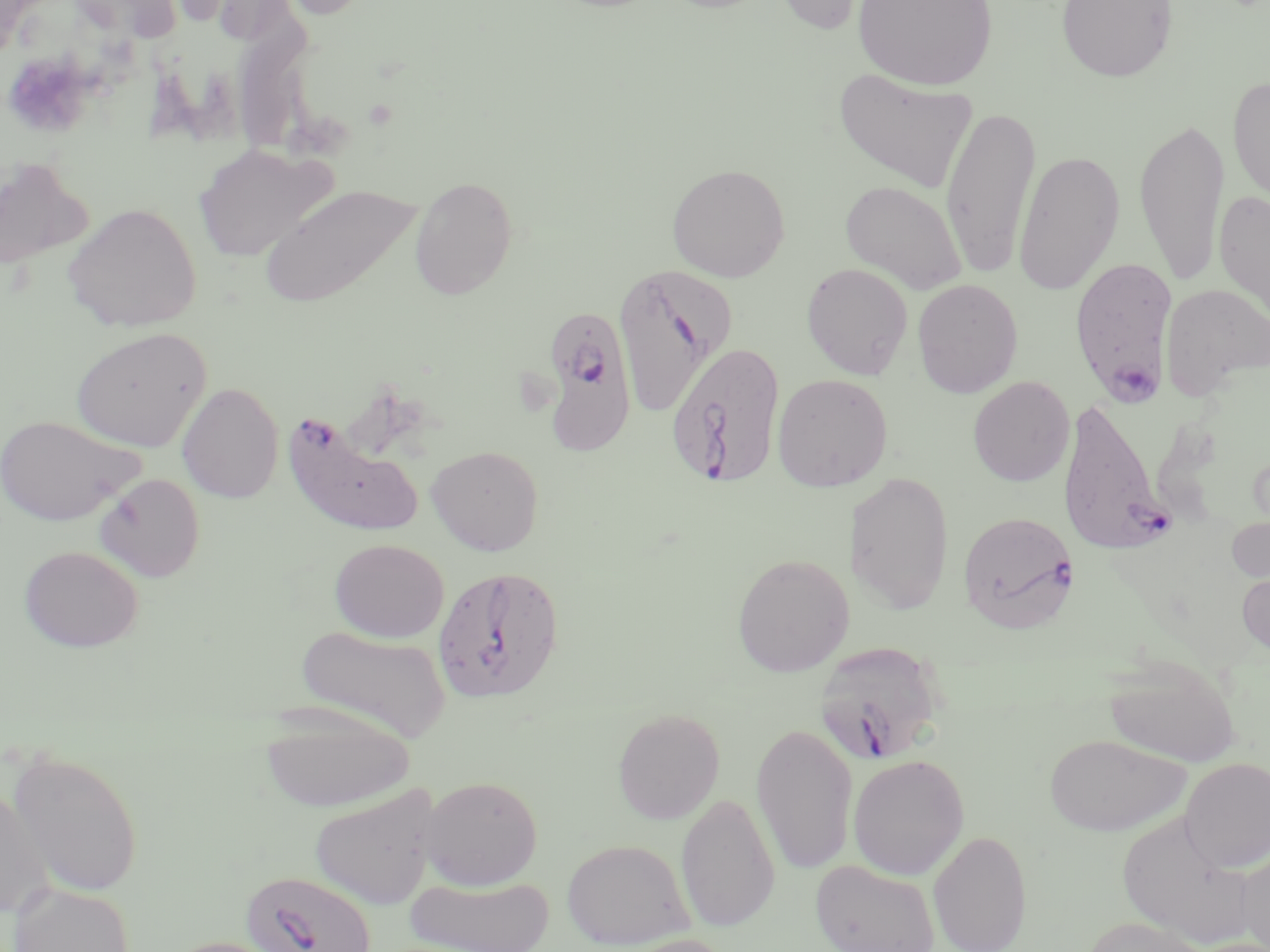

Approximate bounding boxes as named x1/y1/x2/y2 corners in pixels. Platelet locations: (x1=3, y1=51, x2=96, y2=137). Plasmodium falciparum-infected red blood cell locations: (x1=1069, y1=256, x2=1178, y2=403), (x1=612, y1=263, x2=736, y2=416), (x1=538, y1=312, x2=644, y2=462), (x1=666, y1=340, x2=787, y2=489), (x1=1057, y1=396, x2=1176, y2=555), (x1=283, y1=414, x2=424, y2=535), (x1=958, y1=510, x2=1080, y2=633), (x1=431, y1=565, x2=565, y2=703), (x1=814, y1=640, x2=947, y2=766), (x1=239, y1=869, x2=377, y2=952). Uninfected red blood cell locations: (x1=67, y1=0, x2=181, y2=42), (x1=768, y1=0, x2=887, y2=35), (x1=853, y1=0, x2=998, y2=90), (x1=1056, y1=0, x2=1177, y2=82), (x1=834, y1=68, x2=978, y2=194), (x1=1228, y1=74, x2=1270, y2=214), (x1=940, y1=105, x2=1041, y2=279), (x1=1134, y1=116, x2=1230, y2=288), (x1=193, y1=143, x2=337, y2=262), (x1=1013, y1=149, x2=1125, y2=297), (x1=0, y1=158, x2=91, y2=271), (x1=667, y1=162, x2=790, y2=281), (x1=409, y1=176, x2=518, y2=300), (x1=841, y1=180, x2=967, y2=294), (x1=261, y1=183, x2=421, y2=308), (x1=1215, y1=188, x2=1270, y2=331), (x1=63, y1=202, x2=201, y2=332), (x1=801, y1=263, x2=913, y2=379), (x1=912, y1=279, x2=1023, y2=398), (x1=1161, y1=283, x2=1270, y2=401), (x1=72, y1=327, x2=211, y2=452), (x1=772, y1=373, x2=893, y2=491), (x1=968, y1=376, x2=1075, y2=487), (x1=177, y1=382, x2=284, y2=503), (x1=0, y1=414, x2=143, y2=526), (x1=426, y1=444, x2=544, y2=556), (x1=848, y1=471, x2=955, y2=614), (x1=94, y1=473, x2=205, y2=582), (x1=1225, y1=506, x2=1270, y2=593), (x1=329, y1=538, x2=449, y2=642), (x1=18, y1=545, x2=144, y2=652), (x1=731, y1=553, x2=854, y2=677), (x1=1237, y1=565, x2=1270, y2=661), (x1=295, y1=624, x2=451, y2=743), (x1=1103, y1=652, x2=1241, y2=768), (x1=259, y1=704, x2=415, y2=812), (x1=612, y1=707, x2=725, y2=824), (x1=751, y1=720, x2=858, y2=877), (x1=1044, y1=733, x2=1188, y2=836), (x1=6, y1=747, x2=145, y2=897), (x1=848, y1=754, x2=969, y2=880), (x1=1180, y1=757, x2=1269, y2=871), (x1=419, y1=775, x2=543, y2=890), (x1=0, y1=783, x2=53, y2=920), (x1=309, y1=784, x2=440, y2=910), (x1=676, y1=793, x2=779, y2=933), (x1=1118, y1=814, x2=1254, y2=945), (x1=928, y1=829, x2=1033, y2=952), (x1=561, y1=838, x2=694, y2=950), (x1=1236, y1=845, x2=1270, y2=952), (x1=810, y1=859, x2=939, y2=952), (x1=406, y1=874, x2=554, y2=951), (x1=9, y1=883, x2=135, y2=952), (x1=1077, y1=916, x2=1215, y2=952), (x1=608, y1=934, x2=735, y2=952), (x1=162, y1=935, x2=297, y2=952). Slide-level diagnosis: Plasmodium falciparum. Thin blood smear. Single field of view. Optical microscopy. May-Grünwald-Giemsa-stained preparation. Image is 1270×952 pixels. Captured at 1000x magnification.